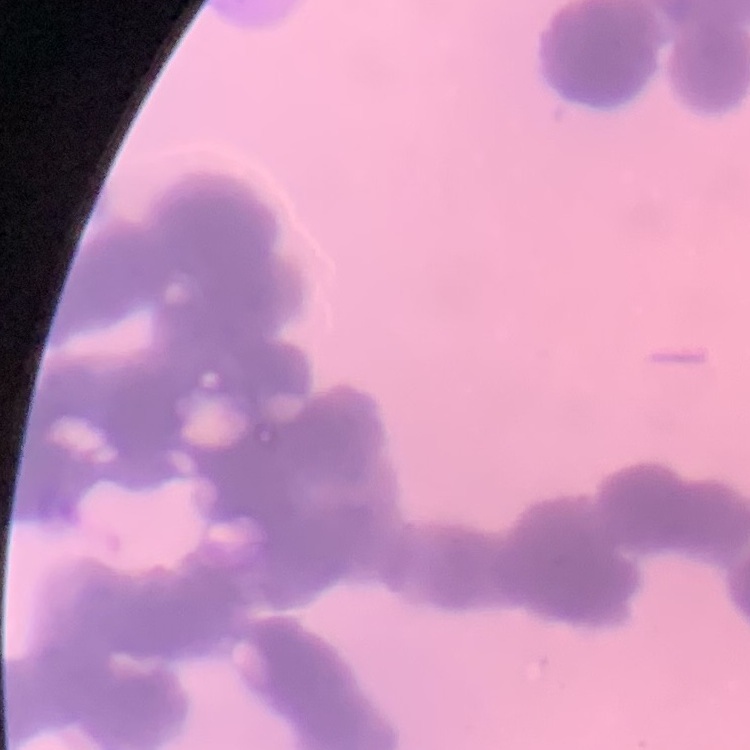

Summary:
  - Red blood cell morphology: rouleaux formation
  - Preparation: thin blood smear
  - Stain: Field's or Giemsa
  - Image type: one tile cut from a larger photomicrograph